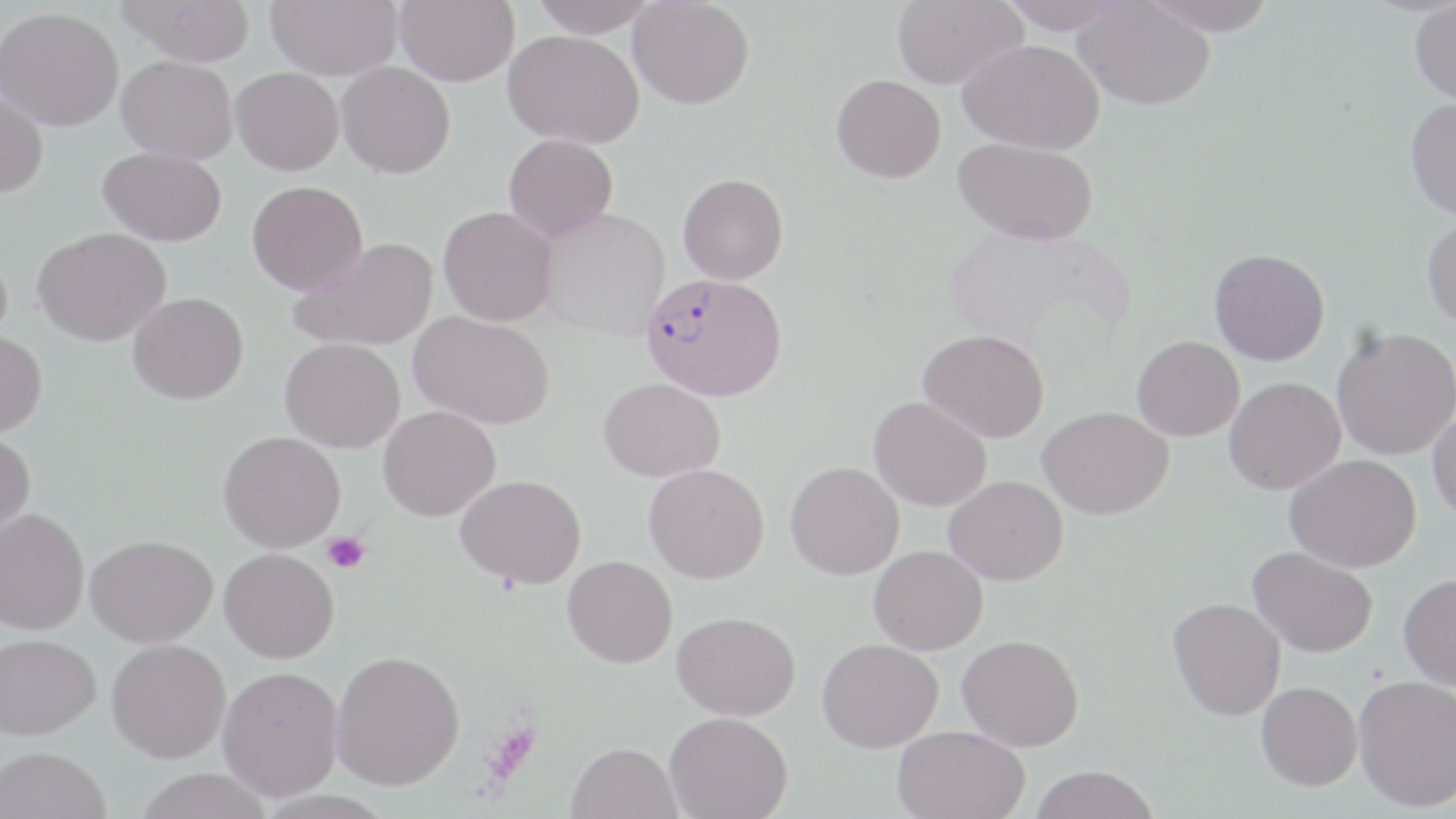

Approximate bounding boxes as (x1,y1)-(x2,y2) corner pairs in pixels. Plasmodium falciparum-infected red blood cell locations: (640,271)-(788,402). Uninfected red blood cell locations: (117,0)-(255,66), (266,0)-(403,80), (394,0)-(519,86), (530,0)-(660,38), (628,0)-(755,109), (891,0)-(1027,89), (997,0)-(1132,34), (1138,0)-(1277,36), (1073,1)-(1215,110), (1410,2)-(1456,105), (0,7)-(124,131), (503,29)-(644,149), (957,38)-(1104,154), (116,55)-(238,164), (336,61)-(455,178), (230,67)-(344,175), (831,74)-(946,183), (0,88)-(49,198), (1405,97)-(1456,221), (503,133)-(618,241), (953,137)-(1099,244), (97,146)-(227,246), (678,173)-(789,285), (247,180)-(368,295), (438,205)-(558,326), (536,207)-(670,340), (1421,215)-(1456,332), (947,223)-(1135,356), (33,227)-(172,346), (288,237)-(439,352), (0,246)-(12,351), (1208,248)-(1330,366), (128,291)-(249,405), (409,311)-(555,430), (1331,326)-(1456,461), (918,329)-(1049,443), (0,331)-(48,437), (1132,335)-(1244,441), (279,337)-(405,453), (1224,376)-(1345,495), (599,377)-(725,483), (869,396)-(991,511), (377,405)-(501,521), (1037,406)-(1173,520), (1428,407)-(1456,525), (0,430)-(36,544), (218,430)-(346,552), (1284,453)-(1421,572), (785,461)-(904,580), (643,463)-(769,583), (455,474)-(586,589), (944,475)-(1068,585), (0,506)-(90,635), (85,534)-(217,647), (869,545)-(988,655), (1248,546)-(1378,658), (219,548)-(339,663), (562,555)-(678,668), (1398,573)-(1456,691), (1168,598)-(1286,721), (672,611)-(800,721), (1,633)-(101,740), (956,634)-(1084,752), (106,638)-(231,763), (816,638)-(942,753), (330,649)-(464,790), (217,665)-(344,801), (1353,675)-(1456,811), (1256,681)-(1362,791), (664,711)-(792,819), (892,725)-(1030,819), (565,741)-(683,819), (0,746)-(111,819), (1029,764)-(1160,819), (134,767)-(275,819). Platelet locations: (322,532)-(370,574), (483,719)-(541,782). Slide-level diagnosis: Plasmodium falciparum. Image is 1456×819 pixels. Optical microscopy. May-Grünwald-Giemsa stain. One field of a larger specimen. 1000x magnification. Thin blood film.